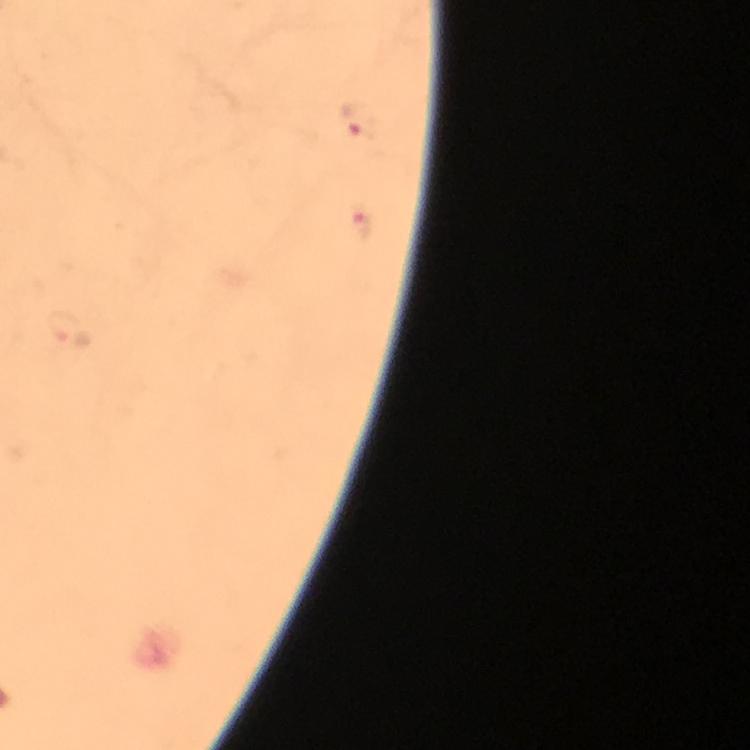 Approximate centers as {x, y} in pixels. Malaria parasite locations: {355, 122}. A crop from one field of view. From a malaria diagnostic workup. Giemsa stain. Thick smear. Image is 750×750 pixels. Immersion oil applied. Photographed with a smartphone mounted on the microscope. At 100x magnification.